Assess for malaria.
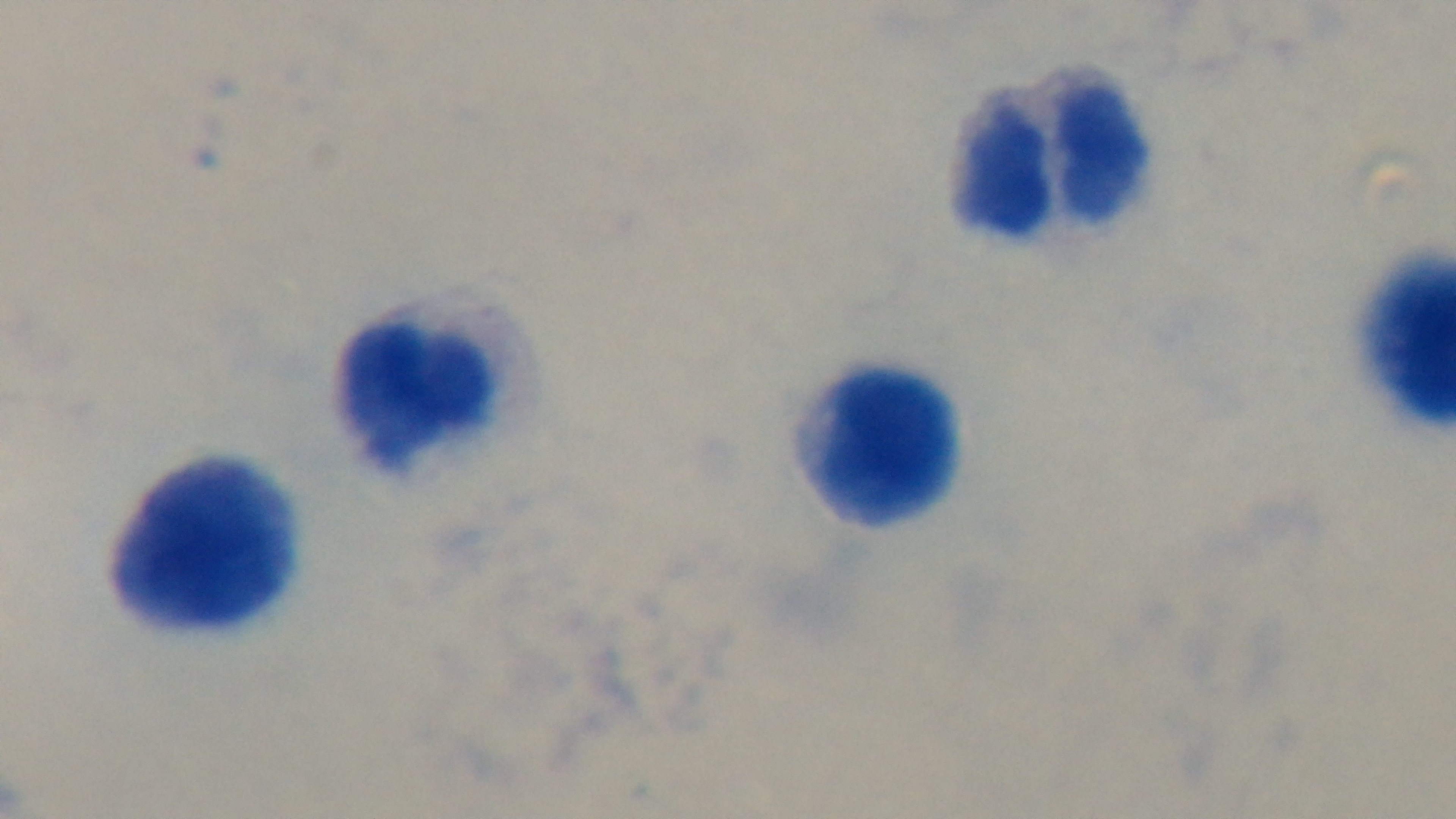
Negative.

{
  "modality": "light microscopy",
  "field_of_view": "single",
  "stain": "Giemsa",
  "objective": "100x oil immersion",
  "preparation": "thick blood film",
  "capture": "mounted 4K digital camera"
}